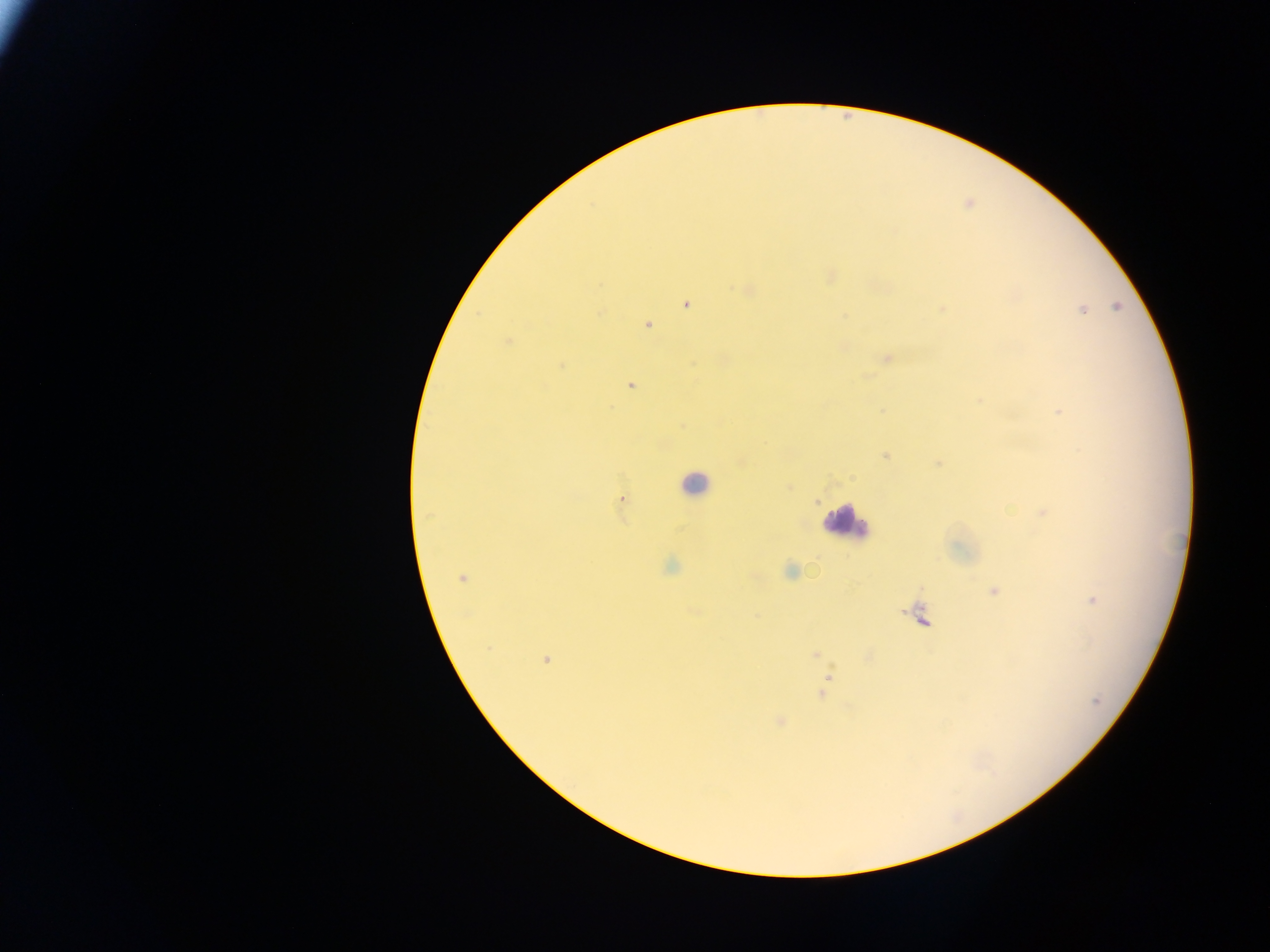
leukocyte locations = approximate centers as [x, y] in pixels: [694, 484], [847, 522]
image size = 1270×952 pixels
capture = mobile-phone photograph through a microscope
preparation = thick blood film
field of view = single
malaria parasite locations = approximate centers as [x, y] in pixels: [742, 290], [686, 305], [1116, 307], [942, 309], [1082, 309], [648, 325], [507, 341], [887, 358], [561, 366], [631, 385], [980, 401], [1060, 412], [885, 456], [939, 464], [620, 499], [1043, 513], [790, 571], [461, 579], [994, 591], [1092, 600], [488, 649], [816, 653], [545, 660], [829, 677], [822, 694], [1097, 700], [780, 722]
country = Ghana